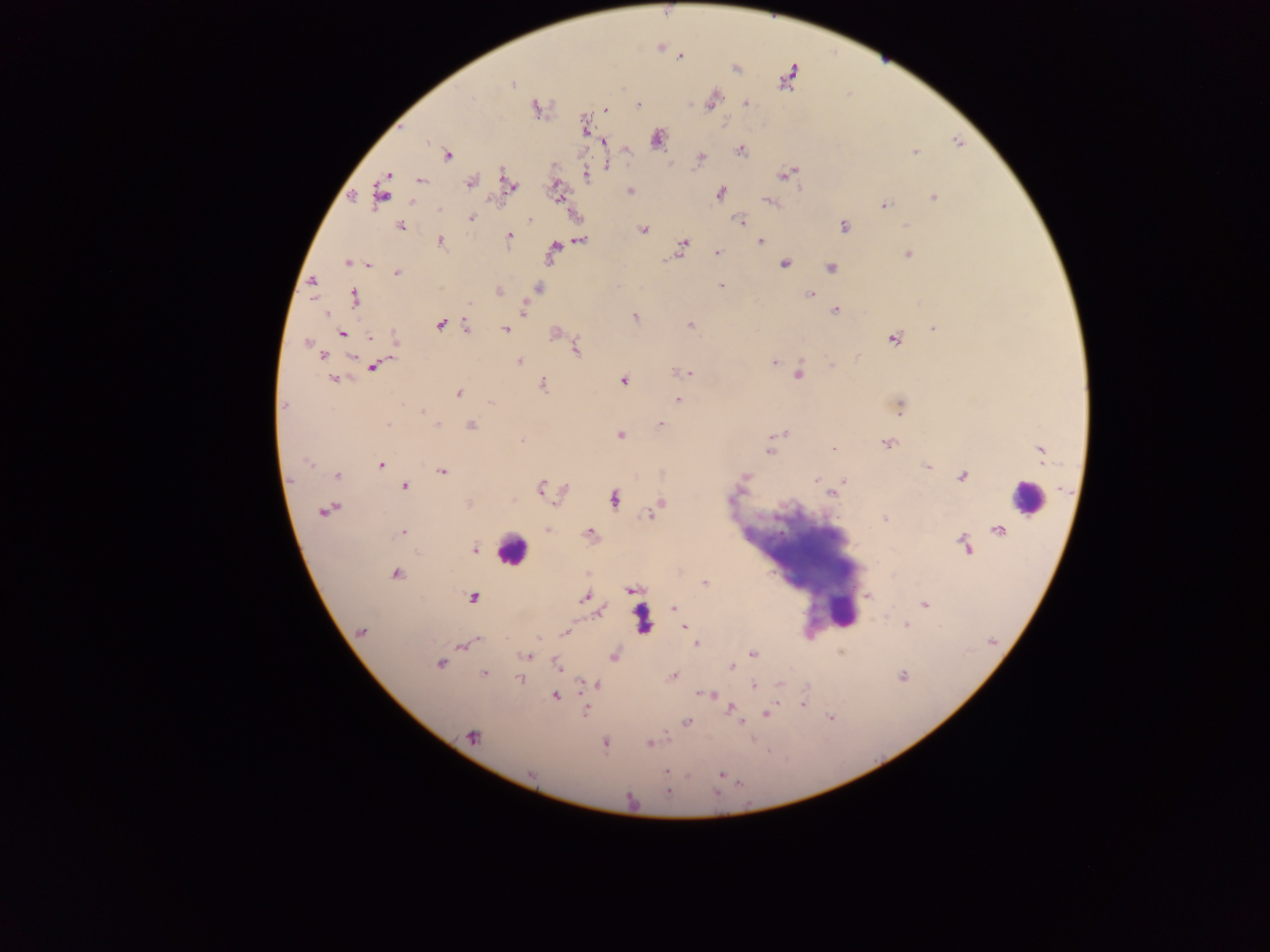

Plasmodium parasite locations = approximate centers as [x, y] in pixels: [679, 57], [735, 68], [787, 77], [512, 85], [713, 101], [638, 104], [747, 104], [536, 109], [605, 109], [584, 126], [658, 139], [603, 142], [741, 150], [916, 151], [448, 155], [700, 158], [606, 165], [786, 174], [389, 175], [586, 175], [421, 180], [470, 182], [509, 183], [630, 191], [720, 193], [382, 195], [934, 198], [770, 202], [884, 206], [471, 218], [529, 219], [740, 221], [401, 226], [844, 226], [907, 226], [643, 229], [509, 237], [582, 240], [440, 241], [760, 241], [682, 246], [554, 249], [717, 253], [908, 255], [347, 262], [367, 264], [784, 264], [830, 268], [397, 272], [312, 282], [721, 286], [539, 288], [498, 291], [810, 294], [354, 297], [471, 304], [836, 310], [523, 311], [327, 314], [635, 317], [440, 325], [691, 325], [466, 327], [933, 327], [506, 330], [342, 334], [370, 337], [894, 339], [395, 340], [307, 342], [576, 349], [322, 356], [352, 357], [857, 358], [519, 361], [773, 363], [832, 365], [373, 367], [687, 373], [799, 374], [334, 380], [623, 381], [543, 385], [458, 393], [678, 399], [490, 403], [284, 405], [900, 406], [422, 411], [389, 425], [438, 425], [471, 425], [661, 425], [782, 434], [620, 435], [522, 441], [887, 444], [833, 450], [770, 451], [1041, 452], [306, 462], [380, 465], [927, 466], [442, 471], [337, 475], [962, 477], [745, 478], [817, 480], [845, 482], [405, 487], [540, 489], [831, 493], [615, 499], [659, 505], [326, 510], [650, 514], [884, 519], [547, 530], [403, 531], [590, 532], [965, 545], [475, 549], [396, 573], [705, 584], [633, 590], [867, 596], [584, 597], [472, 598], [924, 604], [673, 609], [600, 612], [685, 626], [906, 626], [361, 632], [565, 633], [476, 641], [697, 643], [463, 645], [752, 654], [613, 656], [527, 657], [440, 665], [556, 666], [732, 667], [483, 673], [902, 675], [673, 676], [520, 679], [781, 684], [598, 685], [753, 685], [711, 694], [556, 696], [802, 704], [731, 708], [585, 711], [767, 714], [686, 721], [473, 737], [605, 744], [649, 744], [667, 770], [721, 775], [668, 792]
capture = mobile-phone photograph through a microscope
field of view = single
leukocyte locations = approximate centers as [x, y] in pixels: [1026, 498], [511, 551], [842, 612]
image size = 1270×952 pixels
country = Ghana
preparation = thick blood smear